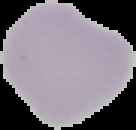
preparation = thin blood smear
result = no Plasmodium parasites seen
image size = 136×130 pixels
image type = cell region segmented out of the field of view; surrounding area masked to black